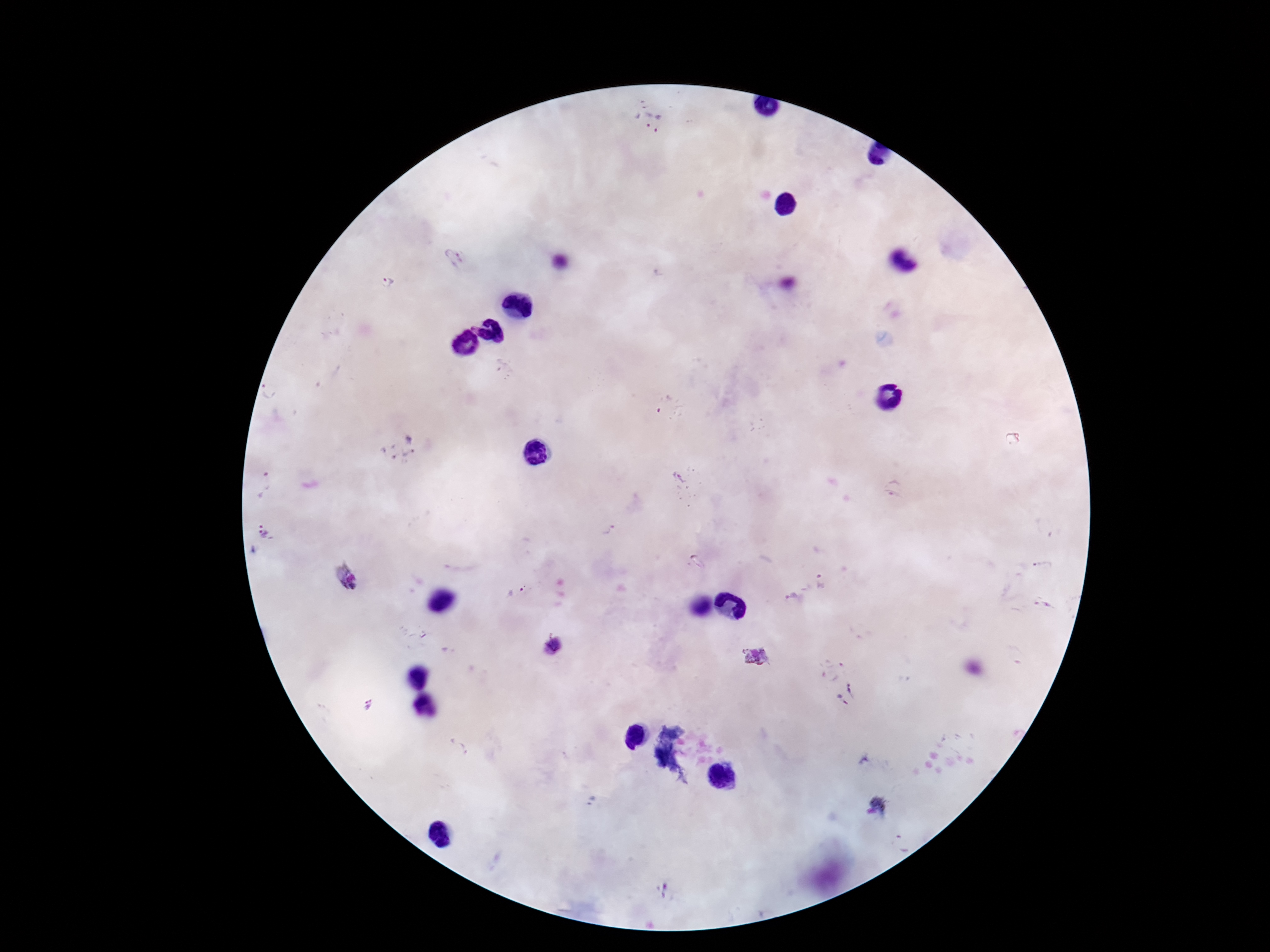

Approximate centers as (x, y) in pixels.
Summary:
  - Plasmodium parasite locations: (637, 118), (662, 124), (453, 259), (388, 283), (666, 408), (399, 449), (681, 479), (264, 485), (893, 488), (608, 529), (266, 532), (1041, 565), (346, 578), (820, 581), (514, 591), (792, 598), (1043, 604), (552, 646), (755, 658), (847, 695), (368, 705), (458, 747), (881, 804), (902, 841), (666, 889)
  - Capture: smartphone camera through the microscope eyepiece
  - Stain: Giemsa
  - Magnification: 100x
  - Field of view: one from this slide
  - Image size: 1270×952 pixels
  - Patient malaria status: infected
  - Preparation: thick blood smear